Assess this cell for malaria.
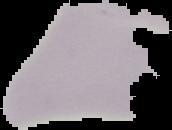
It is uninfected.

Summary:
  - Preparation: thin blood smear
  - Image size: 172×130 pixels
  - Image type: cell region segmented out of the field of view; surrounding area masked to black